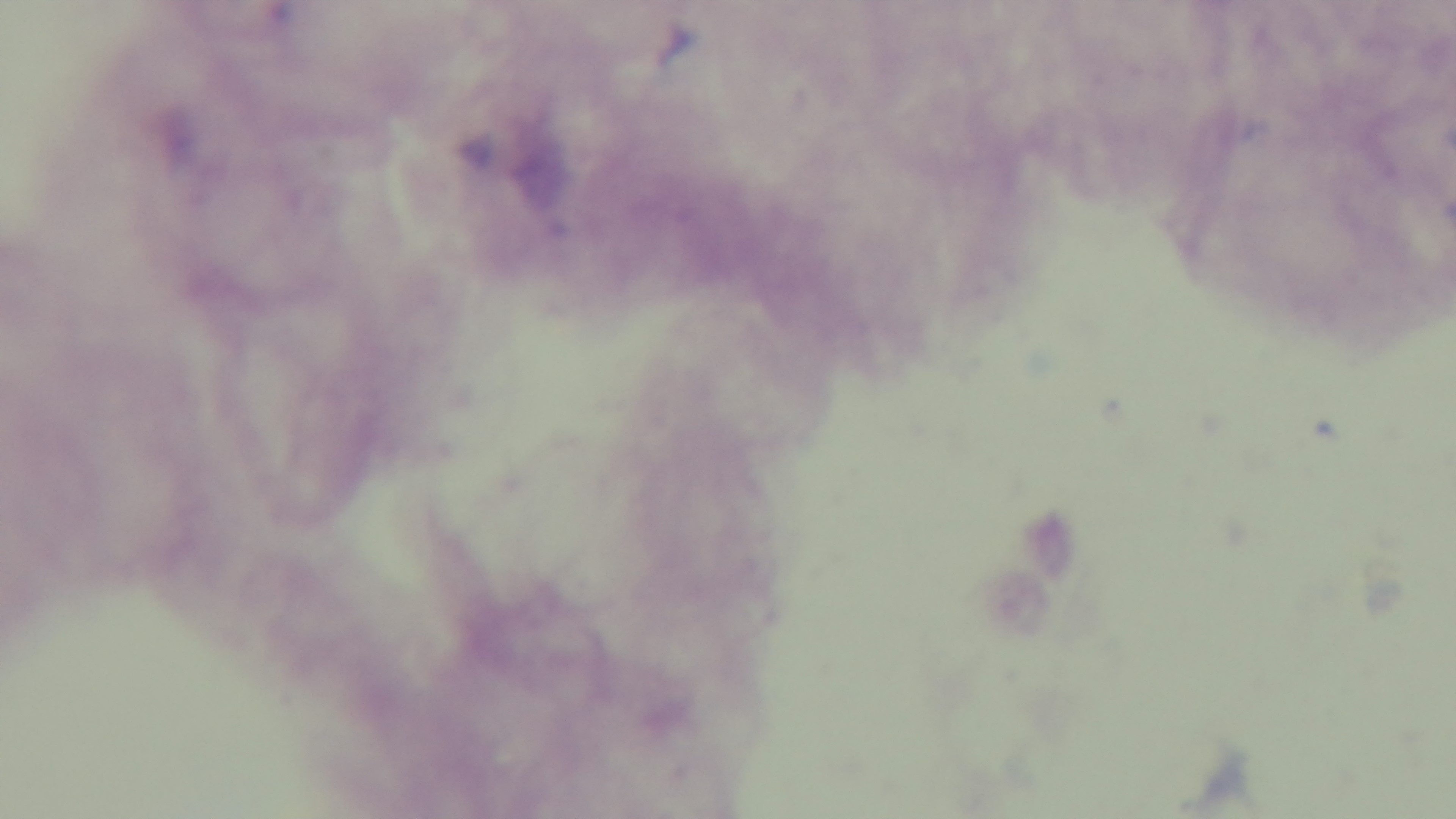
field of view = single
malaria status = negative
stain = Giemsa
modality = light microscopy
objective = 100x oil immersion
preparation = thick blood film
capture = mounted 4K digital camera